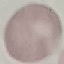
Summary:
  - Result: no malaria parasites detected
  - Capture: smartphone through the microscope eyepiece
  - Preparation: thin blood film
  - Image type: automatically extracted cell patch, resized to 64 × 64 pixels
  - Stain: Giemsa